Comment on the morphology of the erythrocytes.
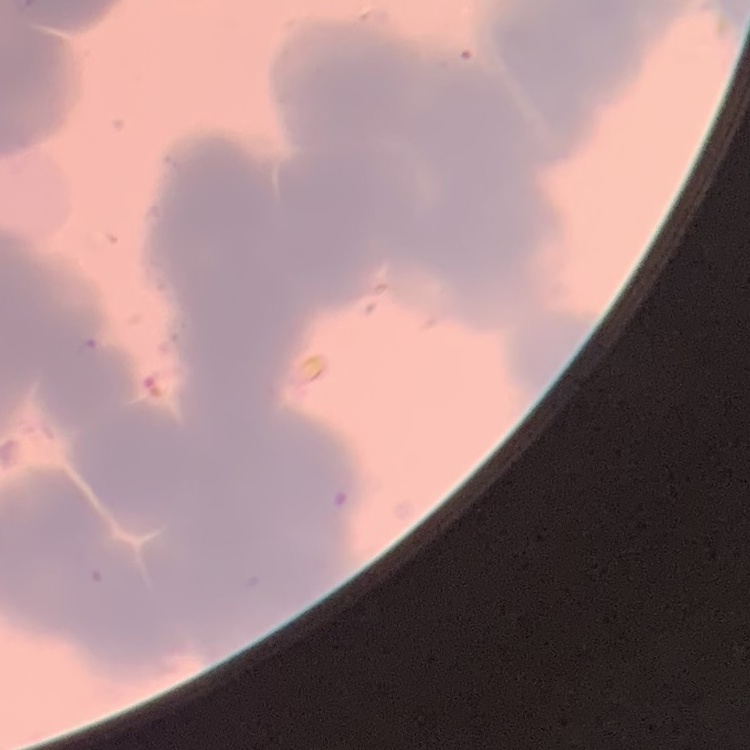

Rouleaux formation.

{
  "preparation": "thin peripheral smear",
  "stain": "Field's or Giemsa",
  "image_type": "one tile cut from a larger photomicrograph"
}